Assess this cell for malaria.
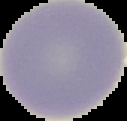

It is uninfected.

Summary:
  - Preparation: thin blood film
  - Image type: cell region segmented out of the field of view; surrounding area masked to black
  - Image size: 127×121 pixels